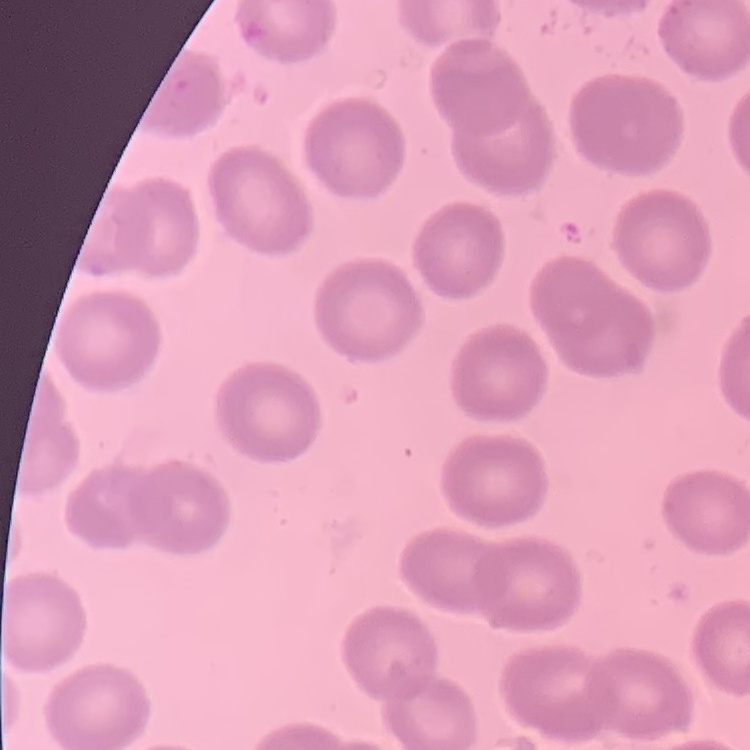
The erythrocytes exhibit no rouleaux formation. Stained with either Field's or Giemsa. Thin peripheral smear. One tile cut from a larger photomicrograph.